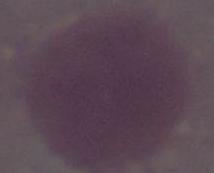
modality = photomicrograph
identification = erythrocyte
magnification = 1000x